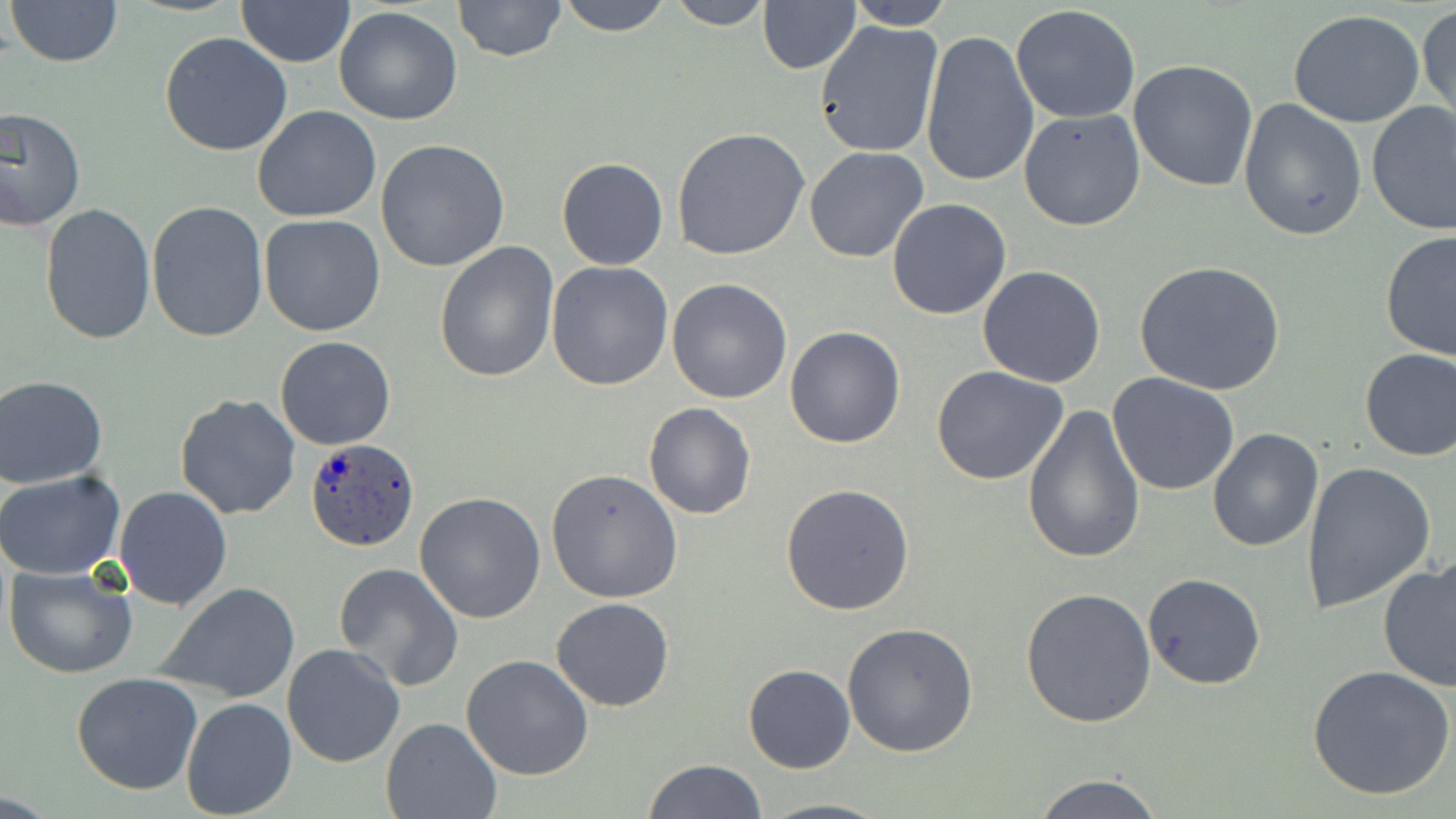
Summary:
  - Coordinate format: approximate bounding boxes as named x1/y1/x2/y2 corners in pixels
  - Uninfected red blood cell locations: (x1=7, y1=0, x2=124, y2=68), (x1=453, y1=0, x2=566, y2=61), (x1=556, y1=0, x2=674, y2=35), (x1=664, y1=0, x2=773, y2=30), (x1=236, y1=1, x2=356, y2=68), (x1=757, y1=1, x2=860, y2=74), (x1=842, y1=1, x2=955, y2=29), (x1=1010, y1=3, x2=1142, y2=125), (x1=1417, y1=3, x2=1455, y2=126), (x1=334, y1=6, x2=463, y2=125), (x1=1287, y1=10, x2=1428, y2=129), (x1=813, y1=20, x2=944, y2=159), (x1=918, y1=29, x2=1038, y2=190), (x1=159, y1=34, x2=293, y2=156), (x1=1128, y1=59, x2=1260, y2=192), (x1=1238, y1=98, x2=1367, y2=240), (x1=1367, y1=101, x2=1456, y2=234), (x1=252, y1=106, x2=383, y2=223), (x1=1, y1=107, x2=86, y2=232), (x1=1019, y1=109, x2=1147, y2=230), (x1=672, y1=128, x2=811, y2=261), (x1=375, y1=139, x2=510, y2=271), (x1=804, y1=146, x2=929, y2=263), (x1=556, y1=157, x2=669, y2=270), (x1=886, y1=198, x2=1013, y2=320), (x1=39, y1=202, x2=155, y2=344), (x1=145, y1=203, x2=268, y2=343), (x1=258, y1=215, x2=386, y2=337), (x1=1380, y1=230, x2=1456, y2=361), (x1=435, y1=240, x2=560, y2=382), (x1=546, y1=260, x2=674, y2=390), (x1=1135, y1=260, x2=1287, y2=398), (x1=977, y1=264, x2=1107, y2=387), (x1=666, y1=277, x2=794, y2=404), (x1=784, y1=326, x2=906, y2=448), (x1=275, y1=336, x2=396, y2=450), (x1=1358, y1=347, x2=1456, y2=461), (x1=932, y1=364, x2=1070, y2=485), (x1=1107, y1=372, x2=1240, y2=497), (x1=0, y1=376, x2=111, y2=488), (x1=175, y1=392, x2=303, y2=520), (x1=644, y1=402, x2=755, y2=519), (x1=1021, y1=402, x2=1146, y2=564), (x1=1207, y1=428, x2=1323, y2=552), (x1=1300, y1=462, x2=1436, y2=616), (x1=547, y1=467, x2=683, y2=602), (x1=1, y1=469, x2=126, y2=580), (x1=780, y1=483, x2=915, y2=615), (x1=114, y1=485, x2=232, y2=609), (x1=413, y1=492, x2=547, y2=624), (x1=1377, y1=557, x2=1456, y2=693), (x1=3, y1=563, x2=137, y2=679), (x1=333, y1=563, x2=464, y2=690), (x1=1142, y1=572, x2=1266, y2=690), (x1=157, y1=584, x2=299, y2=703), (x1=1020, y1=588, x2=1156, y2=728), (x1=550, y1=598, x2=674, y2=712), (x1=476, y1=619, x2=666, y2=762), (x1=842, y1=623, x2=979, y2=758), (x1=281, y1=643, x2=407, y2=768), (x1=462, y1=654, x2=594, y2=781), (x1=743, y1=663, x2=855, y2=774), (x1=1308, y1=665, x2=1456, y2=801), (x1=70, y1=671, x2=202, y2=794), (x1=180, y1=697, x2=297, y2=819), (x1=381, y1=716, x2=503, y2=818), (x1=644, y1=759, x2=766, y2=818), (x1=1032, y1=772, x2=1166, y2=817), (x1=759, y1=796, x2=892, y2=818)
  - Plasmodium ovale-infected red blood cell locations: (x1=304, y1=438, x2=420, y2=552)
  - Slide-level diagnosis: Plasmodium ovale
  - Preparation: thin blood smear
  - Modality: light microscopy
  - Stain: May-Grünwald-Giemsa
  - Image size: 1456×819 pixels
  - Field of view: single
  - Magnification: 1000x